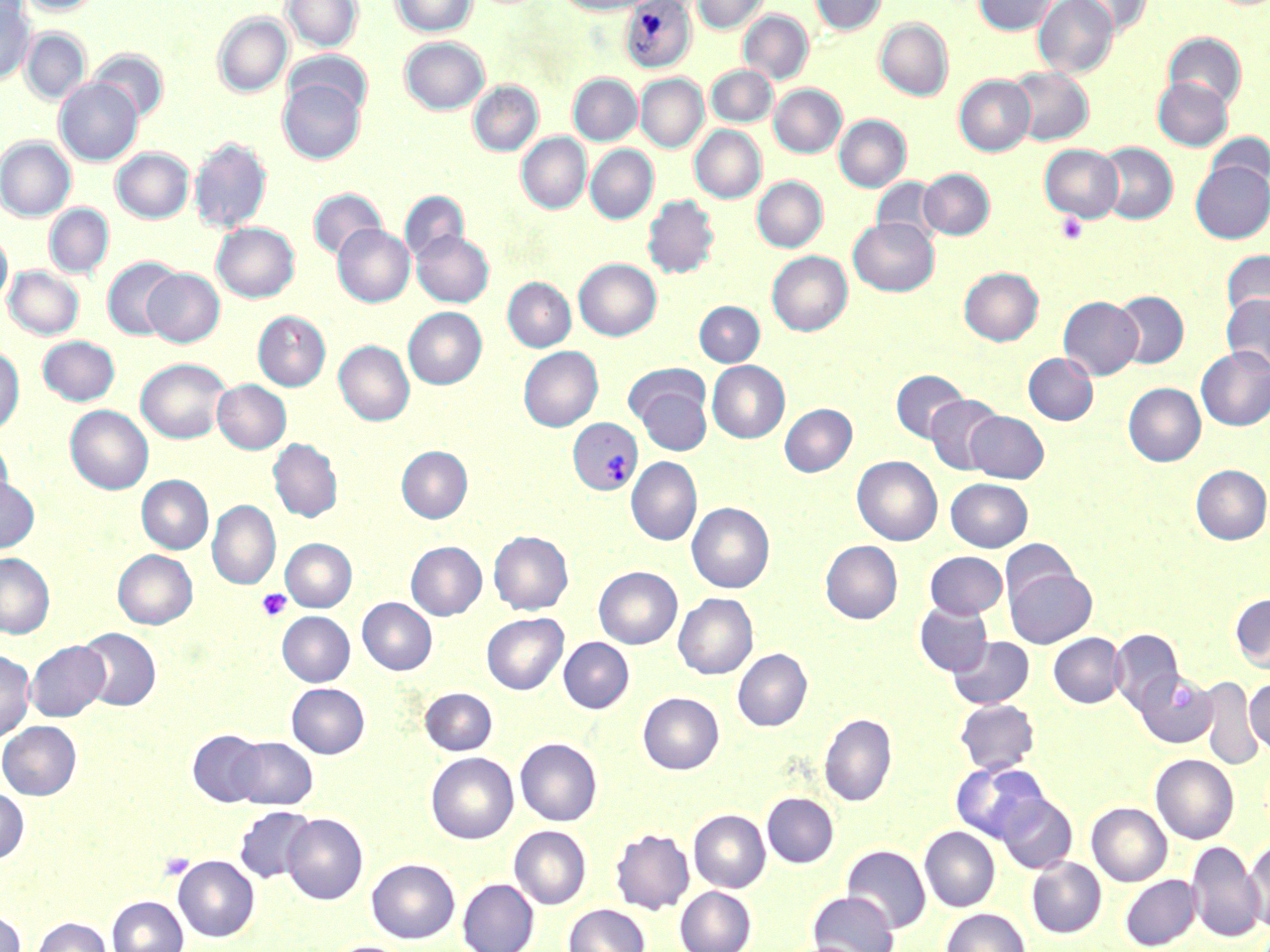

slide_level_diagnosis: Plasmodium vivax
field_of_view: one of a larger specimen
image_size: 1270×952 pixels
preparation: thin blood film
platelet_locations: 'approximate bounding boxes as (x1,y1)-(x2,y2) corner pairs in pixels: (1055,212)-(1089,245), (257,588)-(291,621), (160,853)-(194,880)'
plasmodium_vivax_infected_red_blood_cell_locations: 'approximate bounding boxes as (x1,y1)-(x2,y2) corner pairs in pixels: (619,1)-(697,74), (568,417)-(642,495)'
stain: May-Grünwald-Giemsa
modality: light microscopy
magnification: 1000x
uninfected_red_blood_cell_locations: 'approximate bounding boxes as (x1,y1)-(x2,y2) corner pairs in pixels: (18,0)-(104,15), (282,0)-(362,52), (392,0)-(477,36), (555,0)-(656,15), (693,0)-(768,34), (811,0)-(886,35), (974,0)-(1057,35), (1034,0)-(1118,78), (1069,0)-(1152,37), (0,2)-(34,85), (739,11)-(813,84), (213,13)-(292,97), (875,19)-(953,100), (22,29)-(90,104), (1163,32)-(1247,110), (400,37)-(489,114), (88,50)-(169,123), (286,50)-(372,118), (706,65)-(777,127), (1006,66)-(1093,146), (568,74)-(642,145), (636,74)-(708,153), (954,75)-(1035,156), (1153,77)-(1232,150), (55,78)-(143,166), (278,78)-(365,164), (468,82)-(542,156), (769,84)-(846,157), (834,115)-(911,192), (690,125)-(766,203), (1205,132)-(1269,196), (517,133)-(591,213), (0,137)-(75,221), (189,137)-(272,234), (1094,143)-(1178,225), (585,145)-(658,224), (1040,145)-(1123,222), (111,148)-(193,223), (1191,161)-(1270,243), (919,168)-(994,240), (752,176)-(827,252), (871,177)-(944,245), (308,189)-(386,261), (400,191)-(468,265), (643,195)-(720,278), (44,204)-(113,278), (849,218)-(939,296), (213,222)-(299,302), (333,224)-(414,307), (412,230)-(493,307), (0,233)-(12,309), (1221,250)-(1270,323), (767,251)-(852,336), (102,258)-(182,340), (574,258)-(661,340), (4,266)-(83,339), (143,268)-(224,347), (959,268)-(1043,345), (503,278)-(575,352), (1111,290)-(1188,368), (1221,294)-(1270,372), (1058,296)-(1143,380), (694,301)-(765,366), (403,307)-(486,389), (253,311)-(330,390), (38,336)-(120,405), (334,340)-(414,425), (0,346)-(24,435), (1196,346)-(1270,431), (518,347)-(603,432), (1023,353)-(1098,425), (137,358)-(231,443), (707,361)-(789,443), (891,370)-(969,443), (213,380)-(291,454), (632,382)-(711,455), (1123,383)-(1206,467), (926,395)-(1005,474), (779,404)-(857,477), (65,406)-(153,495), (965,411)-(1049,482), (268,438)-(342,522), (0,439)-(13,516), (396,446)-(472,523), (852,456)-(942,545), (626,457)-(702,545), (1191,465)-(1270,544), (0,476)-(39,553), (137,476)-(213,553), (946,478)-(1033,551), (207,501)-(280,590), (687,503)-(774,593), (489,531)-(573,614), (281,539)-(356,612), (1000,539)-(1080,610), (821,541)-(902,624), (406,542)-(487,620), (113,550)-(197,629), (925,551)-(1007,618), (0,553)-(54,638), (1005,566)-(1096,648), (594,567)-(682,648), (674,593)-(757,679), (1230,593)-(1270,674), (357,598)-(437,675), (914,601)-(993,677), (277,611)-(355,686), (482,613)-(568,694), (76,628)-(161,711), (1109,629)-(1184,714), (1048,633)-(1125,708), (948,636)-(1034,709), (559,638)-(634,713), (25,640)-(110,721), (733,649)-(812,731), (0,650)-(34,742), (1133,669)-(1217,747), (1196,676)-(1263,770), (1245,678)-(1270,757), (287,683)-(369,758), (420,688)-(497,755), (638,693)-(724,774), (954,699)-(1040,775), (820,713)-(897,806), (0,721)-(81,799), (188,729)-(268,807), (229,736)-(317,810), (515,738)-(602,826), (426,753)-(518,843), (1151,754)-(1239,843), (952,762)-(1049,843), (0,788)-(28,862), (762,793)-(838,867), (996,793)-(1077,874), (1087,803)-(1172,886), (234,806)-(316,884), (689,809)-(770,892), (282,813)-(368,905), (509,825)-(591,908), (920,826)-(1000,912), (610,827)-(695,914), (1245,838)-(1270,934), (1187,840)-(1265,942), (842,845)-(931,933), (173,856)-(259,941), (1027,857)-(1106,938), (366,858)-(460,943), (1121,874)-(1200,949), (457,878)-(539,952), (675,886)-(757,952), (808,891)-(899,952), (107,896)-(187,952), (563,904)-(650,952), (941,908)-(1030,952), (0,911)-(26,952), (32,917)-(111,952), (323,939)-(410,952)'